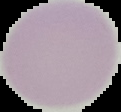
image type = cell region segmented out of the field of view; surrounding area masked to black
image size = 121×112 pixels
malaria status = uninfected
preparation = thin blood smear